Comment on the morphology of the erythrocytes.
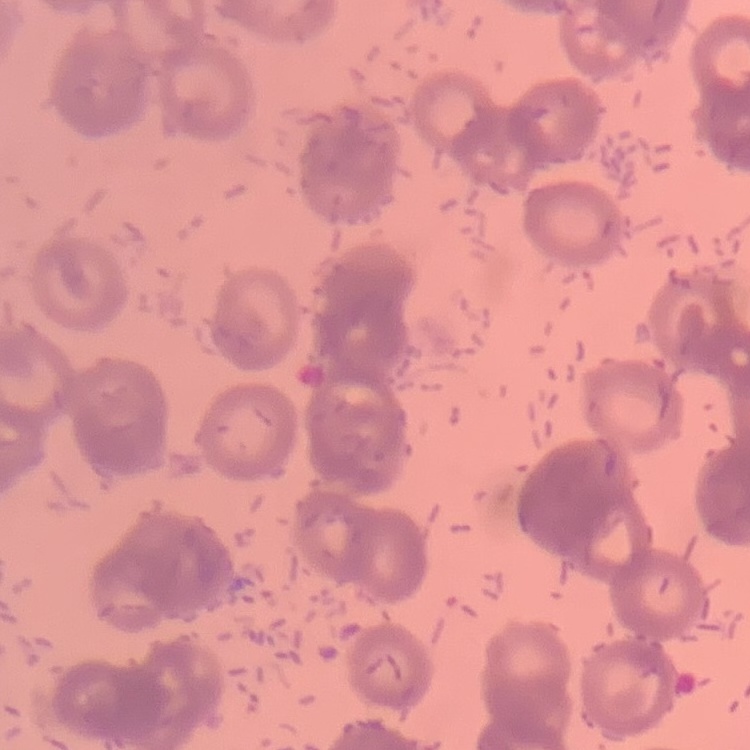

They show rouleaux formation.

Stained with either Field's or Giemsa. Square crop of a larger photomicrograph. Thin blood film.